Classify this cell by malaria status.
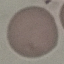
It is uninfected.

{
  "preparation": "thin blood film",
  "image_type": "automatically extracted cell patch, resized to 64 × 64 pixels",
  "capture": "smartphone camera at the microscope eyepiece",
  "stain": "Giemsa"
}